State which parasite is depicted.
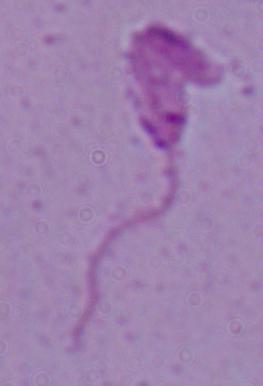

This is Leishmania.

Summary:
  - Magnification: 1000x
  - Modality: micrograph